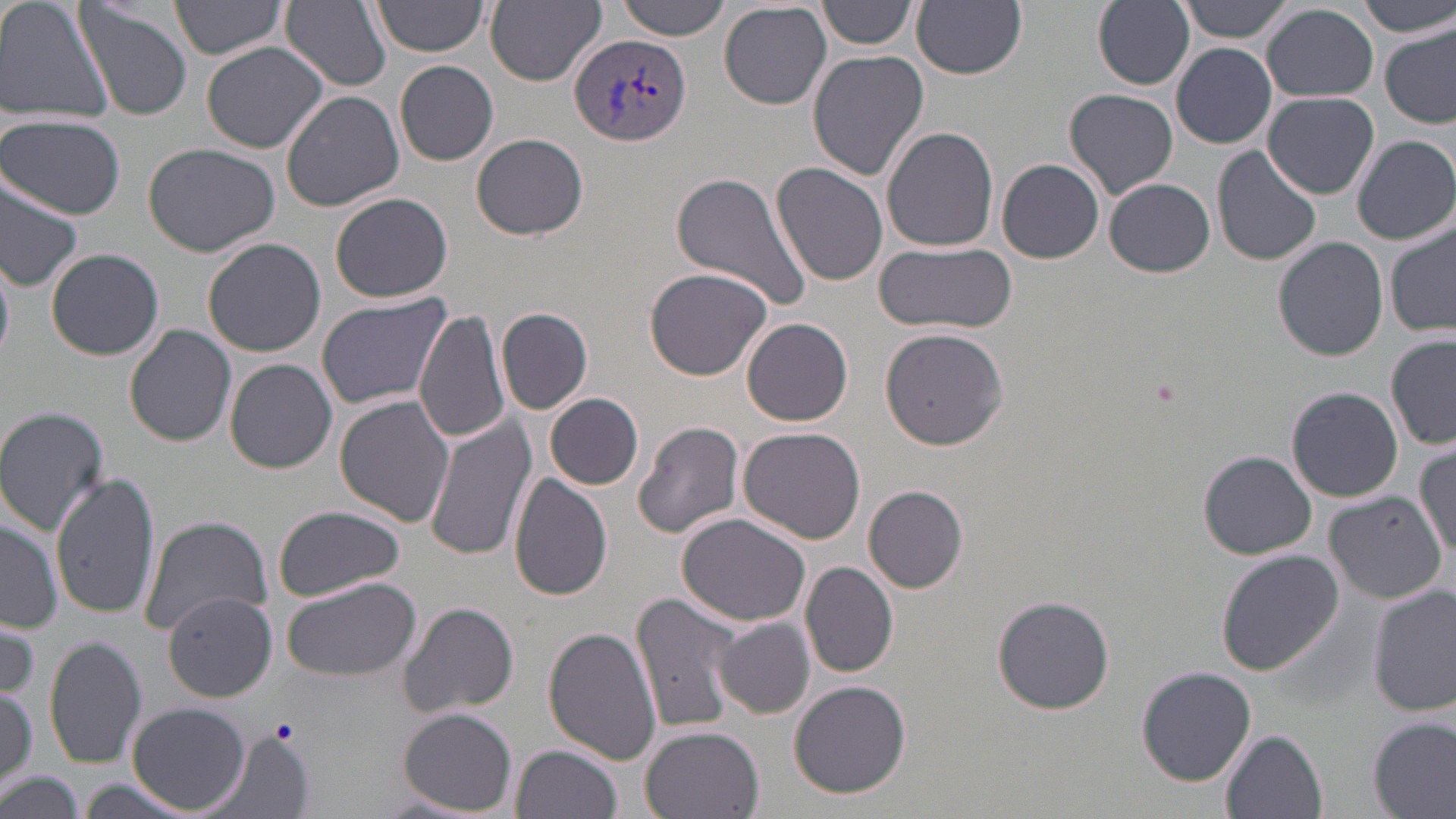
Summary:
  - Coordinate format: approximate bounding boxes as (x1, y1, x2, y2) in pixels
  - Plasmodium vivax-infected red blood cell locations: (568, 32, 691, 149)
  - Uninfected red blood cell locations: (0, 0, 114, 118), (75, 0, 192, 118), (281, 0, 392, 91), (372, 0, 491, 57), (485, 0, 607, 85), (818, 0, 919, 51), (1093, 0, 1195, 89), (1179, 0, 1295, 42), (168, 1, 287, 63), (614, 1, 734, 41), (914, 1, 1027, 78), (1355, 1, 1456, 36), (718, 2, 831, 109), (1263, 4, 1378, 101), (1380, 27, 1455, 128), (200, 41, 330, 153), (1172, 43, 1277, 149), (806, 51, 928, 181), (395, 59, 499, 165), (227, 68, 379, 199), (1064, 88, 1178, 200), (280, 90, 404, 211), (1266, 91, 1379, 198), (0, 116, 128, 219), (881, 125, 999, 252), (472, 133, 588, 240), (1353, 136, 1456, 245), (142, 140, 281, 257), (1212, 145, 1320, 268), (997, 158, 1104, 264), (770, 161, 888, 286), (670, 170, 813, 313), (0, 177, 83, 292), (1104, 178, 1214, 277), (330, 193, 456, 304), (1385, 224, 1456, 339), (203, 237, 327, 355), (1274, 237, 1389, 360), (873, 241, 1018, 335), (47, 248, 164, 360), (0, 255, 14, 366), (644, 267, 772, 380), (316, 295, 450, 412), (497, 307, 593, 414), (415, 308, 512, 444), (741, 318, 853, 426), (125, 324, 238, 447), (880, 327, 1009, 449), (1386, 336, 1456, 451), (225, 359, 337, 473), (1287, 387, 1405, 502), (545, 392, 644, 490), (334, 396, 455, 527), (0, 406, 111, 534), (423, 417, 536, 564), (633, 422, 745, 542), (737, 426, 866, 544), (1412, 445, 1456, 555), (1198, 450, 1317, 559), (50, 470, 160, 618), (509, 473, 614, 601), (863, 485, 969, 593), (1323, 493, 1448, 604), (272, 506, 404, 601), (676, 512, 810, 626), (139, 516, 271, 636), (0, 518, 63, 632), (1217, 550, 1343, 675), (802, 562, 899, 678), (283, 577, 421, 682), (1369, 584, 1455, 715), (633, 591, 743, 738), (163, 593, 277, 701), (992, 594, 1115, 715), (398, 601, 520, 718), (2, 611, 40, 699), (713, 620, 816, 717), (546, 626, 664, 765), (44, 636, 147, 769), (1137, 666, 1256, 785), (789, 681, 911, 798), (0, 685, 38, 786), (129, 703, 251, 815), (397, 708, 519, 813), (1369, 714, 1455, 817), (638, 725, 767, 819), (204, 729, 311, 819), (1221, 729, 1327, 819), (514, 744, 623, 819), (0, 770, 83, 819), (72, 779, 198, 816)
  - Slide-level diagnosis: Plasmodium vivax
  - Preparation: thin blood smear
  - Magnification: 1000x
  - Modality: light microscopy
  - Field of view: single
  - Stain: May-Grünwald-Giemsa
  - Image size: 1456×819 pixels